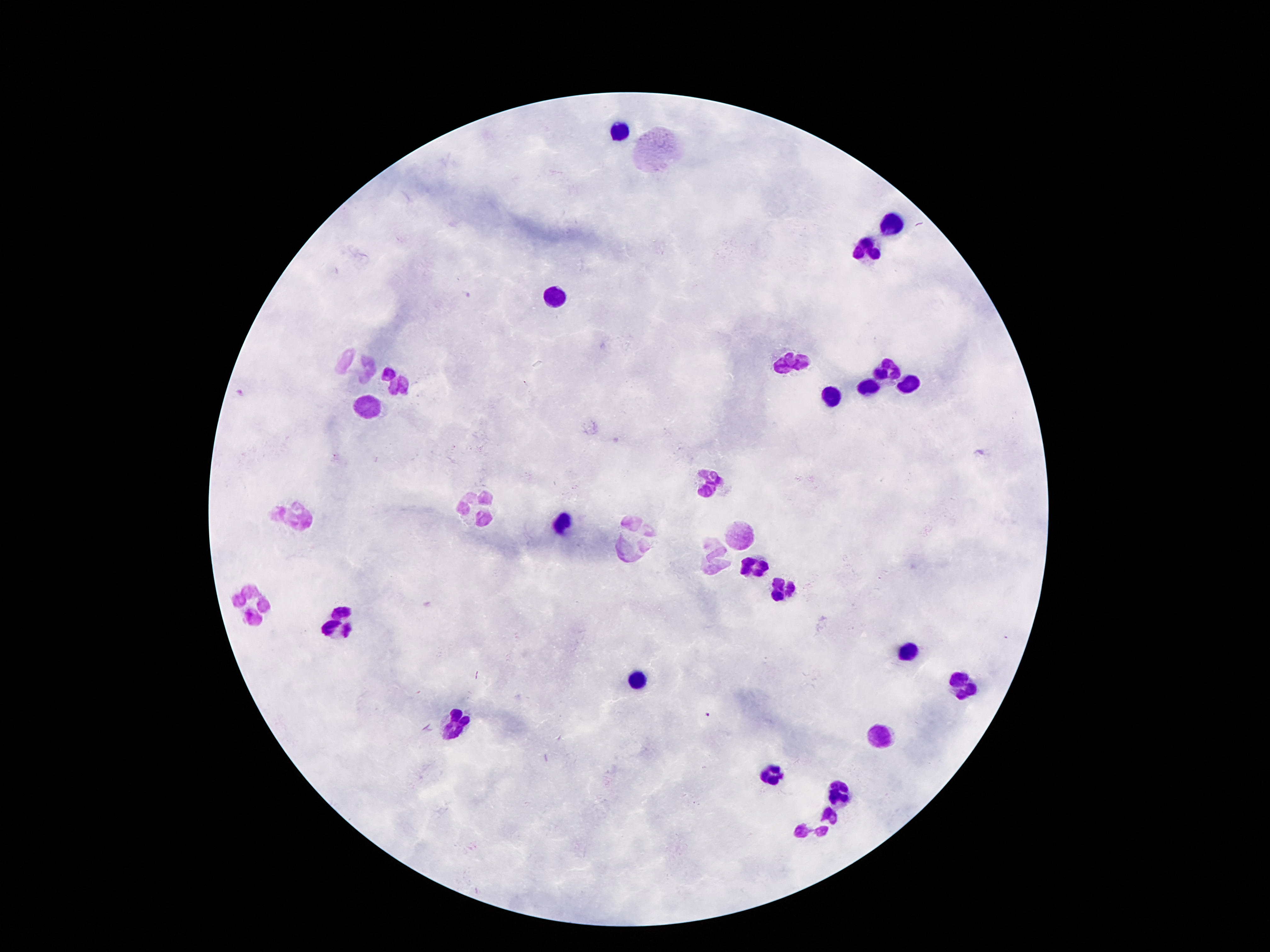
Approximate centers as {x, y} in pixels. Leukocyte locations: {621, 129}, {894, 223}, {868, 247}, {551, 297}, {789, 359}, {361, 364}, {891, 367}, {397, 382}, {907, 382}, {868, 387}, {833, 395}, {368, 407}, {712, 483}, {480, 507}, {294, 516}, {560, 523}, {744, 531}, {632, 539}, {714, 557}, {756, 568}, {781, 587}, {254, 602}, {336, 622}, {908, 653}, {637, 678}, {963, 685}, {455, 724}, {880, 736}, {772, 776}, {837, 793}, {819, 822}. Single field of view. 100x magnification. Thick peripheral-blood smear. Image is 1270×952 pixels. Giemsa-stained preparation. Patient malaria status: not infected. Smartphone photograph taken through the microscope eyepiece.